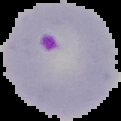

Summary:
  - Image size: 121×121 pixels
  - Preparation: thin blood smear
  - Image type: segmented cell region on a black background
  - Result: Plasmodium parasites identified